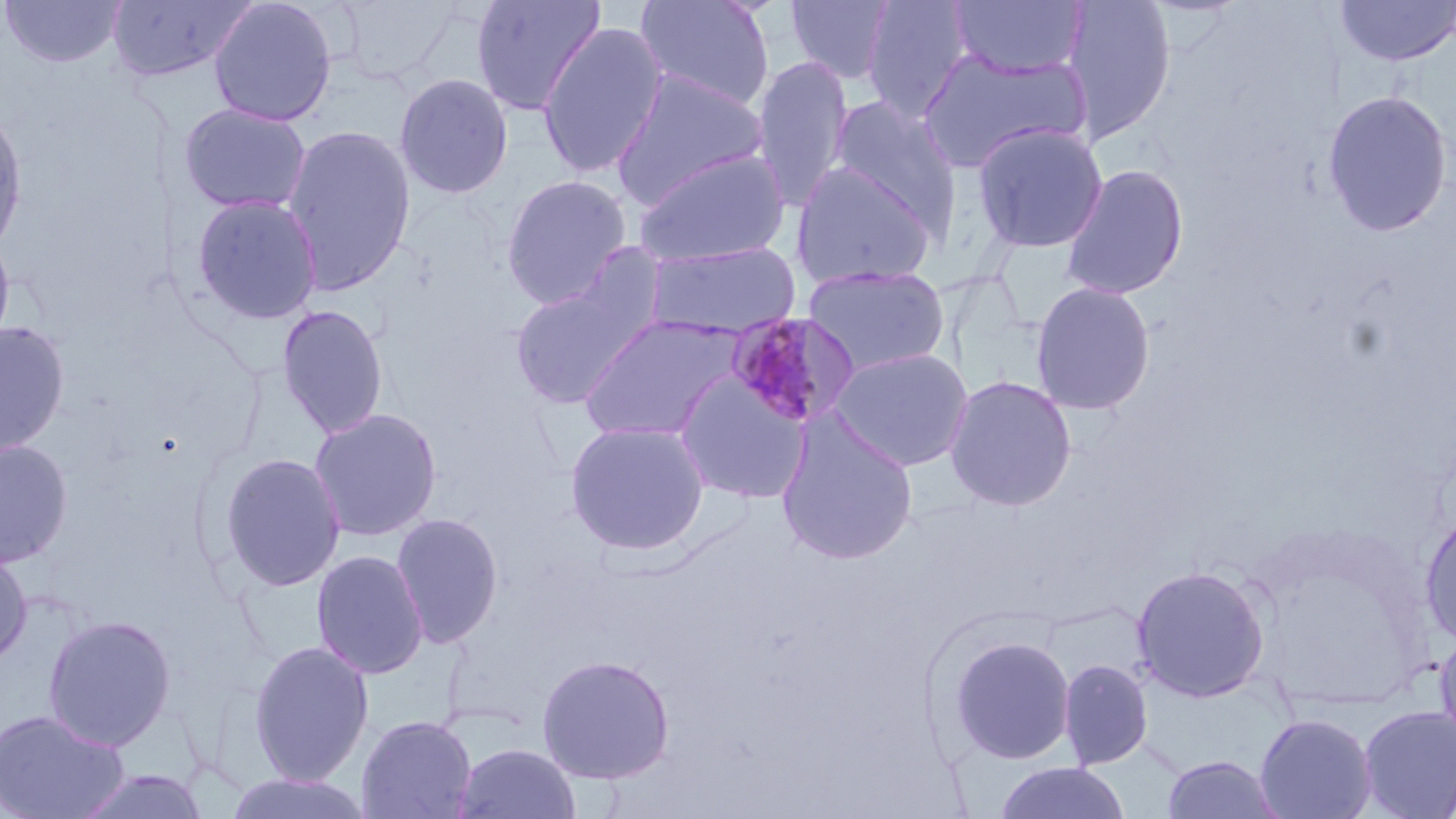

Summary:
  - Coordinate format: approximate bounding boxes as (x1, y1, x2, y2) in pixels
  - Plasmodium malariae-infected red blood cell locations: (725, 310, 861, 429)
  - Uninfected red blood cell locations: (1, 0, 126, 69), (106, 0, 255, 84), (207, 0, 338, 127), (333, 0, 464, 84), (470, 0, 606, 117), (635, 0, 775, 112), (785, 0, 897, 84), (861, 0, 973, 121), (948, 0, 1088, 81), (1061, 0, 1177, 144), (1334, 0, 1456, 67), (536, 22, 669, 179), (918, 47, 1088, 172), (751, 54, 854, 214), (610, 69, 768, 208), (393, 73, 514, 199), (1321, 90, 1453, 237), (828, 97, 961, 233), (178, 102, 312, 215), (0, 105, 28, 259), (971, 122, 1108, 254), (281, 124, 416, 294), (632, 147, 791, 267), (791, 160, 938, 289), (1060, 163, 1189, 300), (500, 174, 633, 308), (190, 193, 323, 325), (0, 228, 16, 360), (643, 240, 802, 339), (508, 263, 663, 411), (803, 264, 951, 377), (1030, 281, 1156, 415), (276, 303, 389, 439), (579, 313, 746, 443), (0, 320, 70, 458), (830, 348, 974, 472), (673, 370, 811, 504), (944, 375, 1077, 511), (308, 408, 443, 542), (774, 412, 918, 566), (565, 420, 710, 555), (0, 439, 74, 568), (216, 452, 347, 593), (390, 512, 504, 649), (1420, 512, 1456, 647), (0, 544, 33, 668), (311, 549, 429, 679), (1130, 565, 1270, 702), (42, 614, 177, 751), (1434, 627, 1456, 753), (946, 635, 1075, 764), (248, 640, 375, 785), (535, 653, 675, 784), (1059, 659, 1152, 769), (1358, 706, 1456, 819), (0, 707, 128, 819), (1254, 713, 1377, 819), (356, 714, 477, 819), (453, 742, 582, 819), (1161, 755, 1284, 818), (994, 762, 1131, 819), (72, 769, 212, 819), (221, 772, 376, 818)
  - Slide-level diagnosis: Plasmodium malariae
  - Modality: light microscopy
  - Preparation: thin blood film
  - Field of view: single
  - Magnification: 1000x
  - Stain: May-Grünwald-Giemsa
  - Image size: 1456×819 pixels